Locate leukocytes (white blood cells).
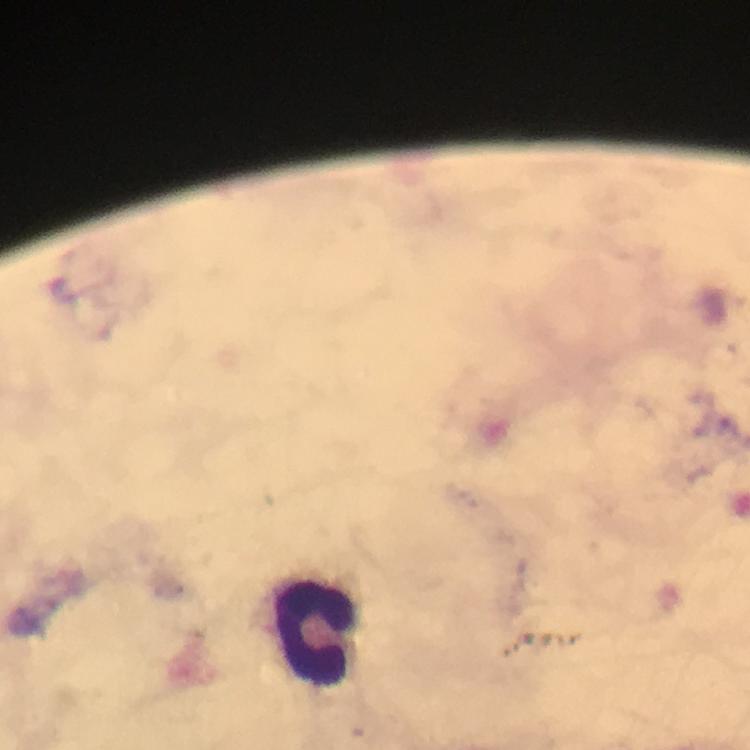
Approximate centers as [x, y] in pixels.
Leukocytes: [316, 632].

stain = Giemsa
magnification = 100x
capture = smartphone photograph through a microscope
cropped from = a single field of view
image size = 750×750 pixels
preparation = thick blood smear
context = from a malaria diagnostic workup
Plasmodium parasites = none detected
immersion oil = applied